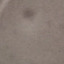

Summary:
  - Result: negative for malaria parasites
  - Stain: Giemsa
  - Capture: smartphone through the microscope eyepiece
  - Image type: cell patch, automatically extracted from a larger field of view and resized to 64 × 64 pixels
  - Preparation: thin smear